Outline each blood parasite and name the species.
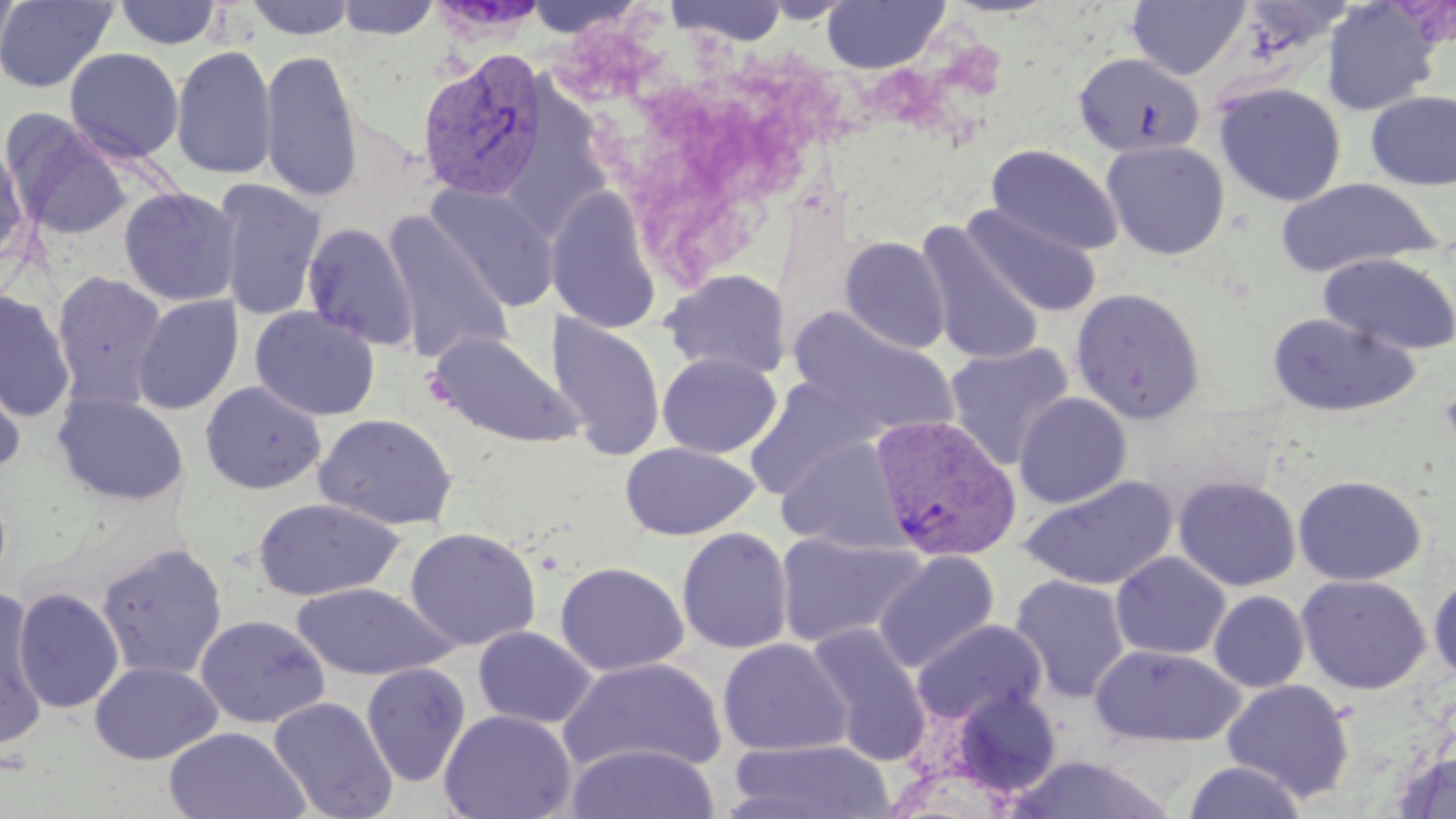
Approximate bounding boxes as [x1, y1, x2, y2] in pixels.
Plasmodium vivax-infected red blood cells: [417, 48, 548, 202], [870, 414, 1022, 563].
No Plasmodium falciparum, Plasmodium ovale, Plasmodium malariae, Babesia divergens, or Trypanosoma brucei observed.

Summary:
  - Platelet locations: [1438, 382, 1456, 459]
  - Uninfected red blood cell locations: [0, 0, 118, 93], [0, 0, 22, 72], [243, 0, 358, 40], [335, 0, 440, 40], [521, 0, 647, 38], [667, 0, 789, 46], [821, 0, 948, 74], [114, 1, 223, 50], [425, 1, 552, 42], [1126, 1, 1251, 81], [1320, 1, 1439, 116], [170, 45, 278, 180], [64, 47, 184, 163], [260, 49, 363, 204], [1073, 52, 1205, 158], [1213, 82, 1347, 207], [1365, 90, 1456, 191], [6, 116, 132, 241], [1101, 140, 1230, 260], [0, 142, 29, 269], [985, 144, 1123, 257], [213, 178, 327, 322], [1273, 178, 1442, 277], [427, 184, 559, 313], [119, 187, 240, 306], [546, 187, 663, 333], [961, 204, 1103, 318], [382, 211, 513, 365], [302, 222, 419, 352], [915, 222, 1048, 367], [839, 236, 950, 354], [1318, 251, 1456, 357], [661, 268, 791, 379], [52, 271, 169, 412], [1070, 286, 1206, 424], [0, 290, 76, 422], [131, 295, 244, 414], [249, 306, 380, 421], [789, 308, 958, 438], [549, 311, 666, 460], [1266, 312, 1422, 417], [428, 331, 583, 450], [944, 343, 1074, 470], [657, 353, 782, 457], [0, 358, 27, 475], [744, 377, 882, 500], [200, 381, 326, 495], [53, 392, 188, 506], [1013, 393, 1132, 508], [313, 413, 458, 531], [777, 436, 908, 552], [619, 443, 759, 541], [1293, 474, 1426, 586], [1021, 475, 1177, 590], [1173, 475, 1301, 592], [252, 497, 405, 602], [404, 526, 542, 651], [676, 526, 793, 654], [775, 531, 929, 649], [96, 542, 228, 681], [873, 551, 1000, 673], [1110, 551, 1231, 660], [554, 561, 689, 677], [1428, 572, 1456, 685], [1009, 574, 1131, 704], [1296, 574, 1431, 694], [290, 582, 457, 682], [13, 587, 124, 714], [0, 589, 49, 752], [1209, 591, 1309, 692], [195, 614, 330, 728], [911, 618, 1048, 726], [805, 622, 930, 764], [472, 625, 597, 729], [717, 638, 852, 757], [1090, 644, 1246, 748], [557, 656, 727, 777], [90, 661, 221, 765], [361, 662, 470, 787], [1221, 679, 1356, 802], [948, 686, 1065, 800], [268, 696, 398, 819], [439, 709, 577, 819], [164, 726, 310, 819], [725, 738, 897, 819], [565, 743, 721, 819], [1390, 750, 1456, 817], [1004, 753, 1178, 818], [1182, 760, 1309, 819]
  - Slide-level diagnosis: Plasmodium vivax
  - Modality: optical microscopy
  - Image size: 1456×819 pixels
  - Field of view: one of a larger specimen
  - Stain: May-Grünwald-Giemsa
  - Preparation: thin blood smear
  - Magnification: 1000x